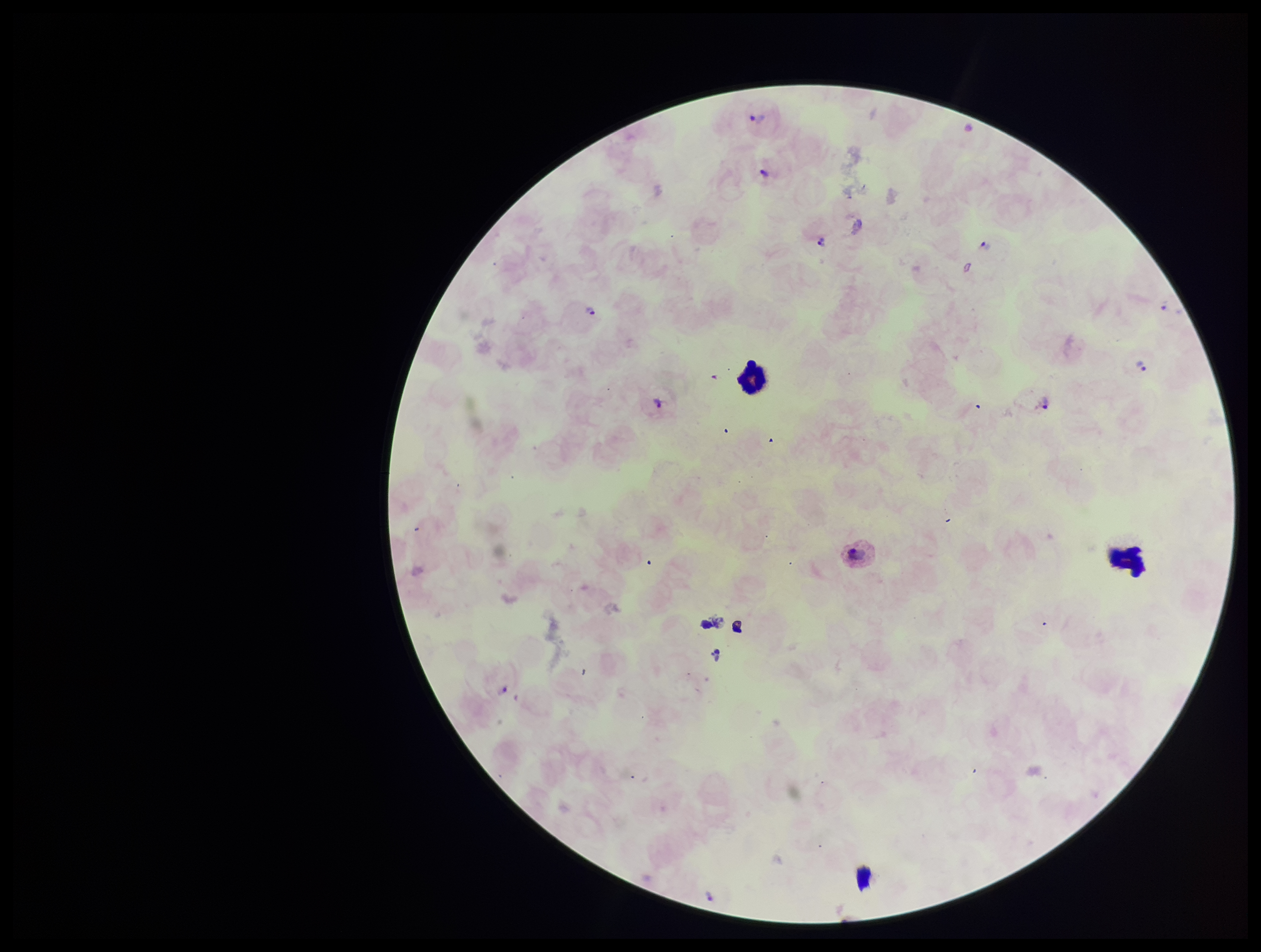

Summary:
  - Image size: 1261×952 pixels
  - Capture: smartphone photograph through the microscope eyepiece
  - Species reported for this patient: Plasmodium vivax
  - Patient malaria status: infected
  - Stain: Giemsa
  - Parasite count: 8
  - Plasmodium parasites: identified
  - Leukocyte count: 2
  - Preparation: thick smear
  - Field of view: one from this slide